Classify this cell by malaria status.
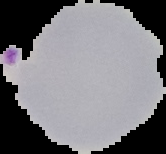

Parasitized.

From a thin blood smear. The area outside the segmented cell region is set to black. Image is 166×154 pixels.